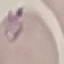
malaria_status: parasitized
stain: Giemsa
image_type: cell patch, automatically extracted from a larger field of view and resized to 64 × 64 pixels
preparation: thin smear
capture: smartphone camera at the microscope eyepiece